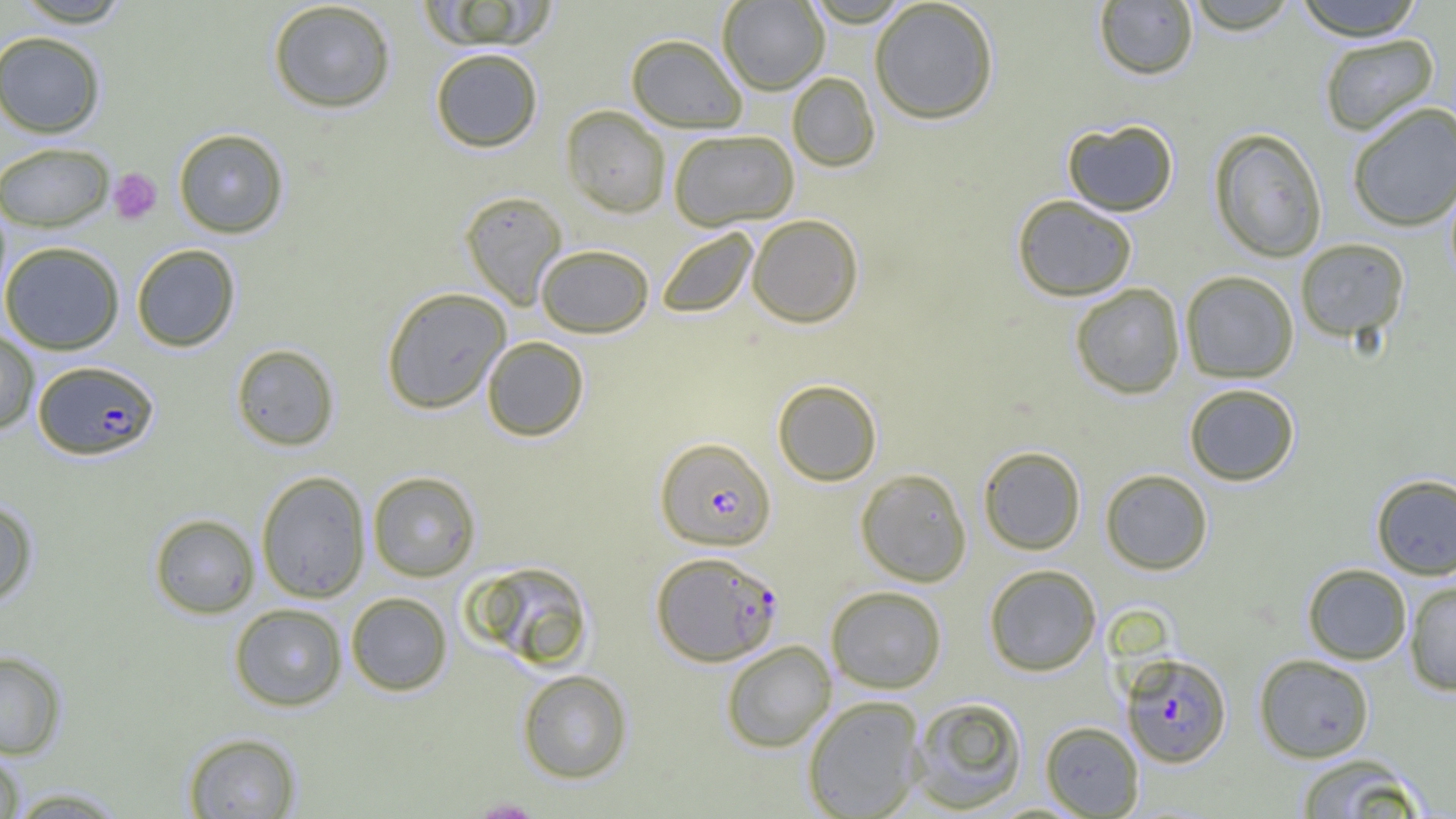 Approximate bounding boxes as (x1, y1, x2, y2) in pixels. Platelet locations: (109, 168, 162, 224). Plasmodium falciparum-infected red blood cell locations (subset): (33, 360, 159, 460), (654, 437, 776, 551), (652, 551, 782, 666), (1121, 653, 1231, 767). Uninfected red blood cell locations (subset): (11, 0, 135, 27), (421, 0, 556, 50), (717, 0, 829, 94), (803, 0, 913, 26), (869, 0, 1000, 124), (1183, 0, 1301, 35), (1293, 0, 1425, 40), (267, 1, 396, 113), (1094, 1, 1199, 80), (0, 30, 106, 138), (1318, 33, 1440, 136), (626, 34, 748, 133), (430, 48, 543, 152), (787, 72, 880, 172), (1346, 101, 1456, 232), (560, 105, 671, 218), (1062, 119, 1179, 216), (173, 128, 289, 238), (1209, 128, 1328, 262), (667, 129, 799, 229), (0, 142, 114, 231), (460, 191, 568, 308), (1012, 195, 1137, 301), (747, 214, 864, 328), (656, 227, 758, 318), (1295, 238, 1409, 341), (0, 241, 124, 354), (131, 244, 240, 351), (535, 244, 654, 337), (1180, 270, 1299, 383), (1070, 283, 1186, 399), (381, 287, 511, 414), (0, 326, 40, 435), (482, 336, 589, 441), (231, 343, 339, 451), (773, 379, 882, 485), (1183, 383, 1300, 486), (978, 446, 1086, 554), (855, 468, 972, 586), (1100, 469, 1213, 575), (256, 471, 371, 603), (367, 471, 481, 582), (1371, 473, 1456, 580), (0, 497, 38, 607), (149, 513, 260, 618), (468, 561, 594, 671), (1302, 563, 1412, 664), (983, 564, 1101, 676), (1404, 579, 1456, 695), (826, 585, 947, 693), (345, 592, 453, 696), (229, 602, 348, 711), (721, 640, 836, 752), (0, 651, 67, 759), (1253, 654, 1375, 762), (517, 668, 633, 783), (802, 695, 926, 819), (909, 695, 1028, 813), (182, 732, 303, 817), (0, 746, 26, 818), (1294, 753, 1425, 819), (4, 786, 131, 818). Slide-level diagnosis: Plasmodium falciparum. Thin blood film. 1000x magnification. Single field of view. Optical microscopy. Image is 1456×819 pixels.